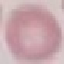

Summary:
  - Malaria status: uninfected
  - Preparation: thin blood film
  - Stain: Giemsa
  - Image type: cell patch, automatically extracted from a larger field of view and resized to 64 × 64 pixels
  - Capture: smartphone camera at the microscope eyepiece